Report the malaria status of this cell.
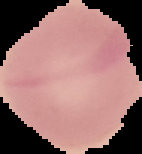
Uninfected.

{
  "image_size": "142×154 pixels",
  "preparation": "thin blood film",
  "image_type": "cell region segmented out of the field of view; surrounding area masked to black"
}